Classify this cell by malaria status.
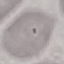
It is uninfected.

stain = Giemsa
capture = smartphone through the microscope eyepiece
image type = cell patch, automatically extracted from a larger field of view and resized to 64 × 64 pixels
preparation = thin smear